Assess this cell for malaria.
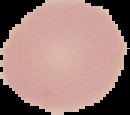

Uninfected.

preparation = thin blood film
image type = segmented cell region with the area outside set to black
image size = 130×115 pixels